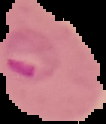

Summary:
  - Preparation: thin blood film
  - Image size: 106×124 pixels
  - Malaria status: parasitized
  - Image type: segmented cell region on a black background